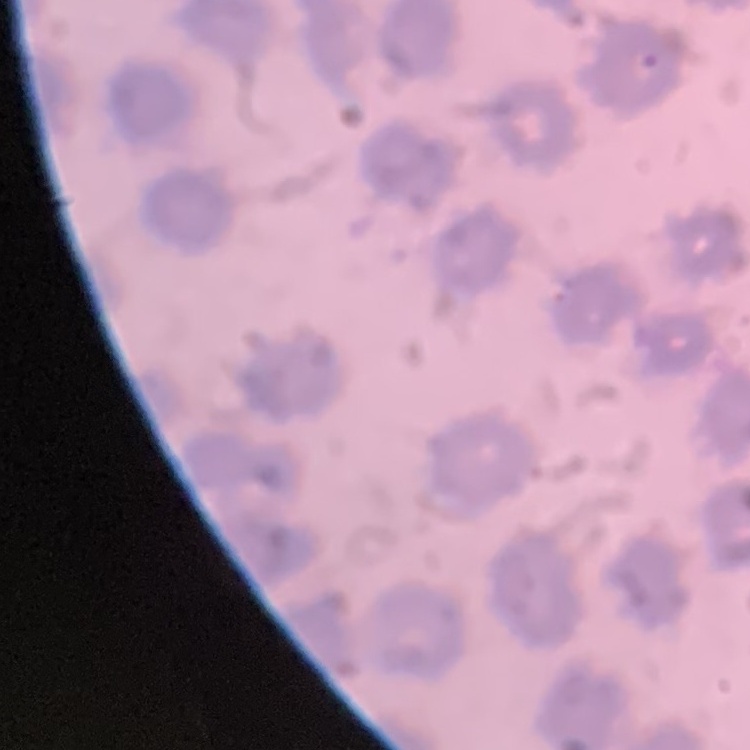

erythrocyte morphology = no rouleaux formation
preparation = thin blood film
image type = one tile cut from a larger photomicrograph
stain = Field's or Giemsa